Assess this cell for malaria.
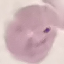
Parasitized.

Thin blood smear. Giemsa stain. Cell patch, automatically extracted from a larger field of view and resized to 64 × 64 pixels. Photographed with a smartphone camera at the microscope eyepiece.